Identify the cell.
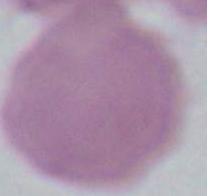
This is an erythrocyte.

modality = photomicrograph
magnification = 1000x